Report the malaria status of this cell.
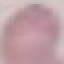

Uninfected.

preparation: thin smear
stain: Giemsa
image_type: cell patch, automatically extracted from a larger field of view and resized to 64 × 64 pixels
capture: smartphone through the microscope eyepiece